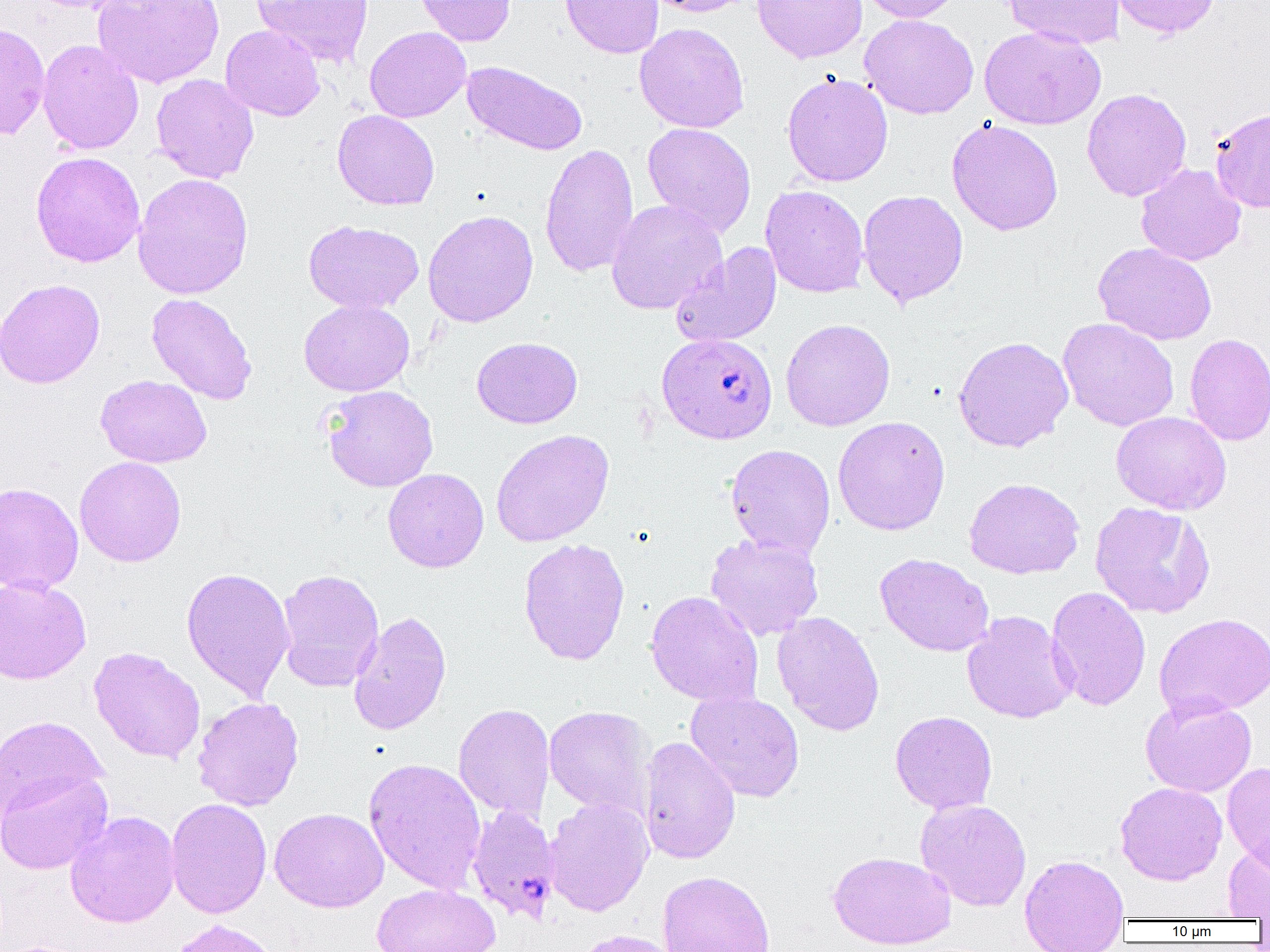
Approximate bounding boxes as named x1/y1/x2/y2 corners in pixels. Plasmodium falciparum-infected red blood cell locations: (x1=656, y1=332, x2=778, y2=444), (x1=466, y1=804, x2=561, y2=922). Uninfected red blood cell locations: (x1=26, y1=0, x2=137, y2=13), (x1=92, y1=0, x2=225, y2=89), (x1=250, y1=0, x2=374, y2=68), (x1=414, y1=0, x2=516, y2=46), (x1=558, y1=0, x2=664, y2=58), (x1=643, y1=0, x2=758, y2=17), (x1=752, y1=0, x2=867, y2=63), (x1=855, y1=0, x2=965, y2=23), (x1=1002, y1=0, x2=1124, y2=49), (x1=1109, y1=0, x2=1221, y2=39), (x1=859, y1=14, x2=979, y2=119), (x1=0, y1=21, x2=50, y2=141), (x1=634, y1=22, x2=750, y2=133), (x1=220, y1=24, x2=325, y2=121), (x1=364, y1=26, x2=471, y2=122), (x1=979, y1=26, x2=1106, y2=130), (x1=37, y1=39, x2=144, y2=155), (x1=462, y1=60, x2=587, y2=156), (x1=782, y1=72, x2=894, y2=187), (x1=151, y1=73, x2=259, y2=184), (x1=1081, y1=88, x2=1192, y2=202), (x1=1209, y1=108, x2=1270, y2=213), (x1=332, y1=109, x2=440, y2=210), (x1=946, y1=119, x2=1063, y2=236), (x1=642, y1=122, x2=757, y2=237), (x1=539, y1=143, x2=639, y2=278), (x1=30, y1=151, x2=146, y2=267), (x1=1135, y1=163, x2=1246, y2=266), (x1=132, y1=172, x2=254, y2=299), (x1=760, y1=185, x2=870, y2=298), (x1=858, y1=189, x2=968, y2=307), (x1=606, y1=199, x2=727, y2=314), (x1=422, y1=210, x2=539, y2=328), (x1=303, y1=219, x2=424, y2=313), (x1=1093, y1=242, x2=1217, y2=346), (x1=670, y1=243, x2=782, y2=348), (x1=0, y1=278, x2=105, y2=389), (x1=146, y1=293, x2=257, y2=405), (x1=299, y1=299, x2=414, y2=396), (x1=1057, y1=317, x2=1179, y2=431), (x1=780, y1=318, x2=896, y2=431), (x1=1184, y1=333, x2=1270, y2=446), (x1=471, y1=336, x2=582, y2=428), (x1=953, y1=336, x2=1074, y2=452), (x1=95, y1=374, x2=212, y2=468), (x1=322, y1=385, x2=439, y2=492), (x1=1111, y1=411, x2=1232, y2=515), (x1=832, y1=416, x2=950, y2=535), (x1=491, y1=429, x2=614, y2=547), (x1=725, y1=443, x2=836, y2=560), (x1=74, y1=456, x2=187, y2=567), (x1=383, y1=468, x2=489, y2=572), (x1=964, y1=477, x2=1085, y2=579), (x1=0, y1=482, x2=84, y2=595), (x1=1089, y1=501, x2=1216, y2=619), (x1=705, y1=532, x2=824, y2=641), (x1=517, y1=537, x2=631, y2=665), (x1=874, y1=553, x2=994, y2=656), (x1=181, y1=566, x2=295, y2=701), (x1=275, y1=568, x2=385, y2=692), (x1=0, y1=575, x2=91, y2=685), (x1=1046, y1=586, x2=1151, y2=711), (x1=645, y1=590, x2=764, y2=707), (x1=348, y1=610, x2=452, y2=736), (x1=962, y1=610, x2=1077, y2=724), (x1=772, y1=611, x2=885, y2=736), (x1=1154, y1=612, x2=1270, y2=720), (x1=87, y1=647, x2=206, y2=764), (x1=686, y1=690, x2=805, y2=802), (x1=1140, y1=696, x2=1257, y2=797), (x1=192, y1=697, x2=304, y2=811), (x1=453, y1=703, x2=555, y2=823), (x1=544, y1=706, x2=654, y2=818), (x1=890, y1=711, x2=997, y2=814), (x1=1, y1=715, x2=107, y2=819), (x1=638, y1=736, x2=741, y2=864), (x1=363, y1=757, x2=487, y2=895), (x1=1222, y1=762, x2=1270, y2=875), (x1=0, y1=768, x2=112, y2=875), (x1=1115, y1=782, x2=1227, y2=886), (x1=543, y1=797, x2=653, y2=917), (x1=165, y1=798, x2=272, y2=919), (x1=915, y1=798, x2=1032, y2=912), (x1=269, y1=807, x2=389, y2=912), (x1=65, y1=810, x2=180, y2=928), (x1=1222, y1=841, x2=1270, y2=920), (x1=828, y1=851, x2=956, y2=950), (x1=1019, y1=854, x2=1130, y2=952), (x1=657, y1=870, x2=776, y2=952), (x1=371, y1=883, x2=501, y2=952), (x1=165, y1=918, x2=283, y2=952), (x1=569, y1=929, x2=683, y2=952). Slide-level diagnosis: Plasmodium falciparum. Thin blood smear. Captured at 1000x magnification. Image is 1270×952 pixels. Single field of view. Light microscopy.